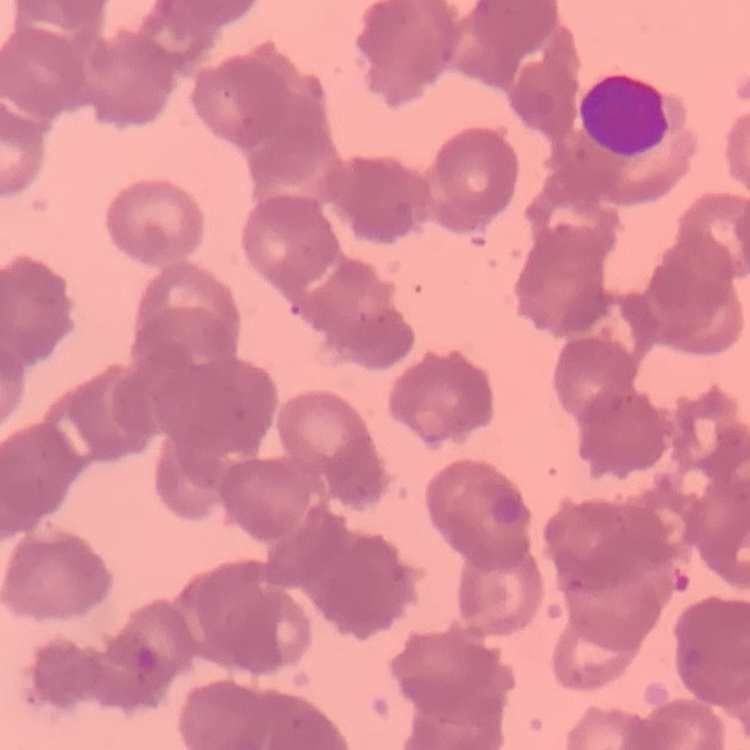

Summary:
  - Red blood cell morphology: rouleaux formation
  - Image type: square crop of a larger photomicrograph
  - Preparation: thin blood film
  - Stain: Field's or Giemsa